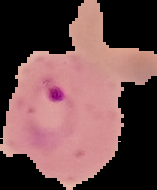
image size = 157×190 pixels
image type = segmented cell region with the area outside set to black
malaria status = parasitized
preparation = thin blood film